Identify the blood parasite species.
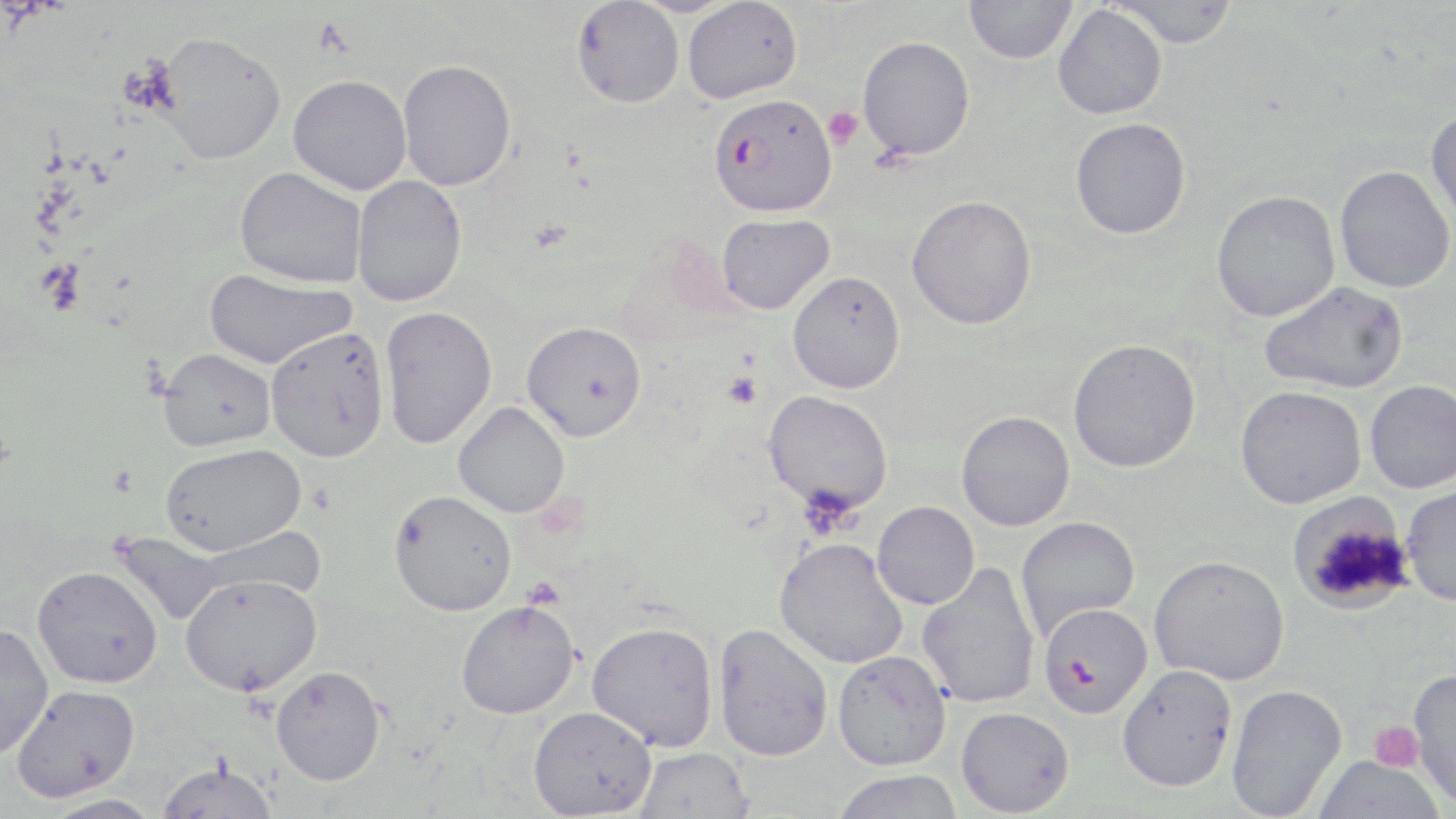
Plasmodium falciparum.

uninfected red blood cell locations = approximate bounding boxes as [x1, y1, x2, y2] in pixels: [964, 0, 1077, 64], [1108, 0, 1241, 47], [571, 1, 684, 108], [682, 1, 802, 104], [1053, 5, 1167, 119], [157, 31, 286, 164], [857, 35, 975, 160], [397, 59, 517, 190], [288, 73, 412, 195], [1425, 108, 1456, 230], [1070, 117, 1190, 239], [1334, 165, 1455, 293], [235, 166, 368, 288], [352, 176, 467, 307], [1211, 190, 1340, 322], [906, 195, 1037, 330], [716, 213, 834, 314], [204, 268, 356, 370], [787, 271, 906, 393], [1258, 280, 1409, 395], [379, 306, 497, 449], [521, 320, 646, 442], [265, 326, 390, 462], [1067, 338, 1201, 472], [158, 347, 276, 451], [1365, 379, 1456, 493], [1235, 385, 1366, 509], [763, 390, 893, 513], [453, 401, 569, 518], [956, 410, 1075, 531], [160, 443, 305, 556], [1400, 483, 1456, 606], [389, 490, 517, 617], [1287, 492, 1416, 615], [872, 501, 979, 609], [1015, 515, 1139, 641], [114, 531, 228, 626], [774, 537, 909, 669], [1149, 555, 1289, 685], [917, 562, 1041, 709], [32, 565, 162, 687], [180, 572, 321, 696], [456, 600, 579, 719], [586, 620, 719, 751], [0, 621, 53, 759], [712, 623, 834, 761], [832, 650, 951, 770], [1117, 664, 1237, 791], [271, 665, 386, 785], [1408, 667, 1456, 809], [1226, 683, 1346, 817], [10, 684, 141, 801], [528, 705, 657, 817], [956, 706, 1074, 816], [634, 747, 754, 819], [1312, 755, 1445, 818], [156, 761, 279, 819], [831, 770, 965, 819], [38, 794, 165, 818]
magnification = 1000x
modality = light microscopy
field of view = one of a larger specimen
preparation = thin blood film
stain = May-Grünwald-Giemsa
Plasmodium falciparum-infected red blood cell locations = approximate bounding boxes as [x1, y1, x2, y2] in pixels: [709, 94, 836, 216], [1038, 602, 1153, 719]
platelet locations = approximate bounding boxes as [x1, y1, x2, y2] in pixels: [821, 106, 863, 149], [37, 259, 86, 314], [724, 372, 761, 408], [1370, 720, 1423, 772]
image size = 1456×819 pixels